Give the position of every leukocyte visible.
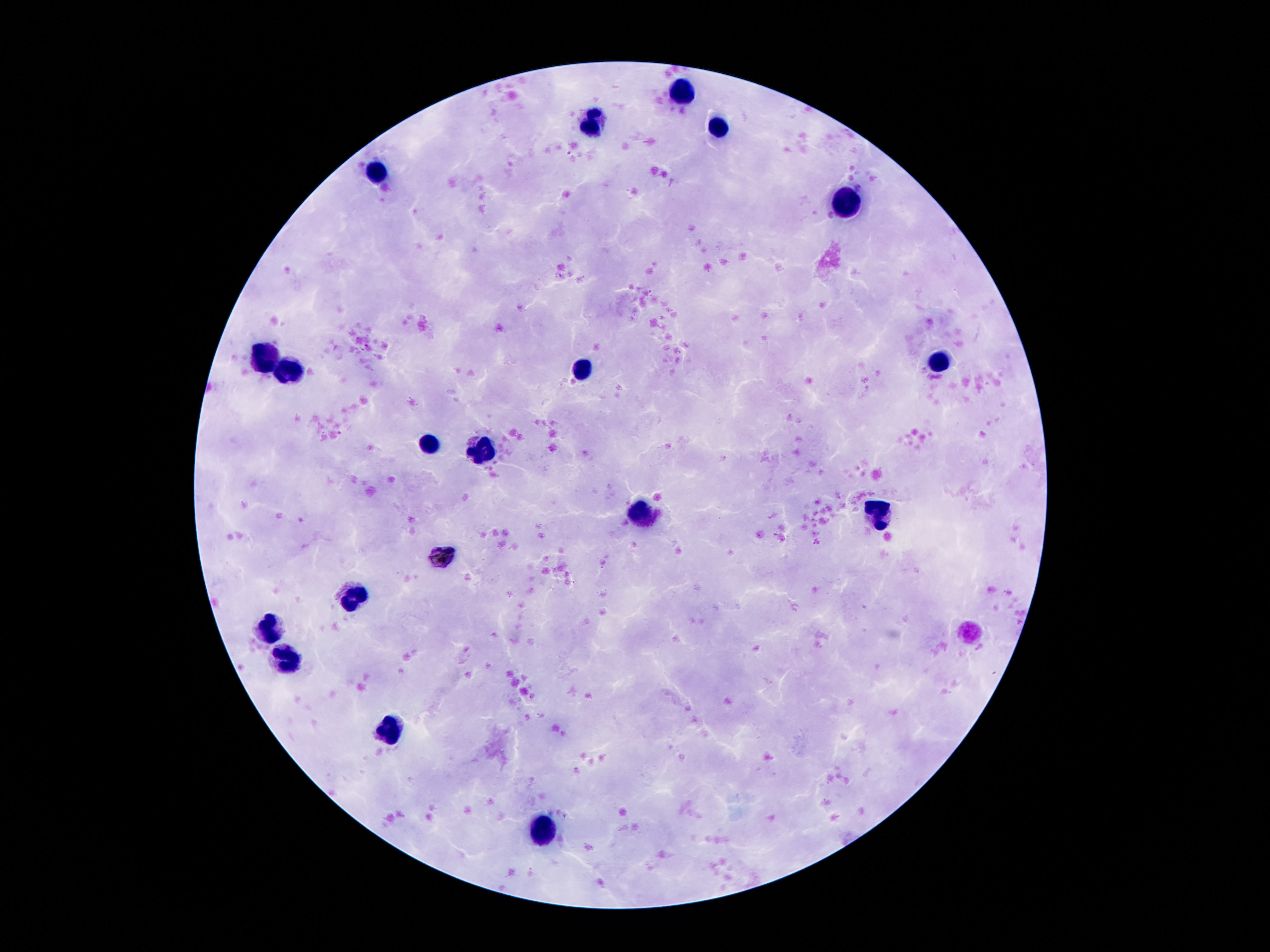

Approximate object centers, in pixels from the top-left corner.
Leukocytes: (x=683, y=93), (x=720, y=126), (x=594, y=127), (x=378, y=172), (x=846, y=202), (x=262, y=357), (x=935, y=364), (x=582, y=371), (x=290, y=373), (x=430, y=444), (x=479, y=452), (x=641, y=511), (x=878, y=511), (x=355, y=593), (x=269, y=628), (x=290, y=658), (x=393, y=731), (x=542, y=832).

field_of_view: one from this slide
image_size: 1270×952 pixels
patient_malaria_status: not infected
preparation: thick blood film
capture: smartphone camera through the microscope eyepiece
magnification: 100x
stain: Giemsa